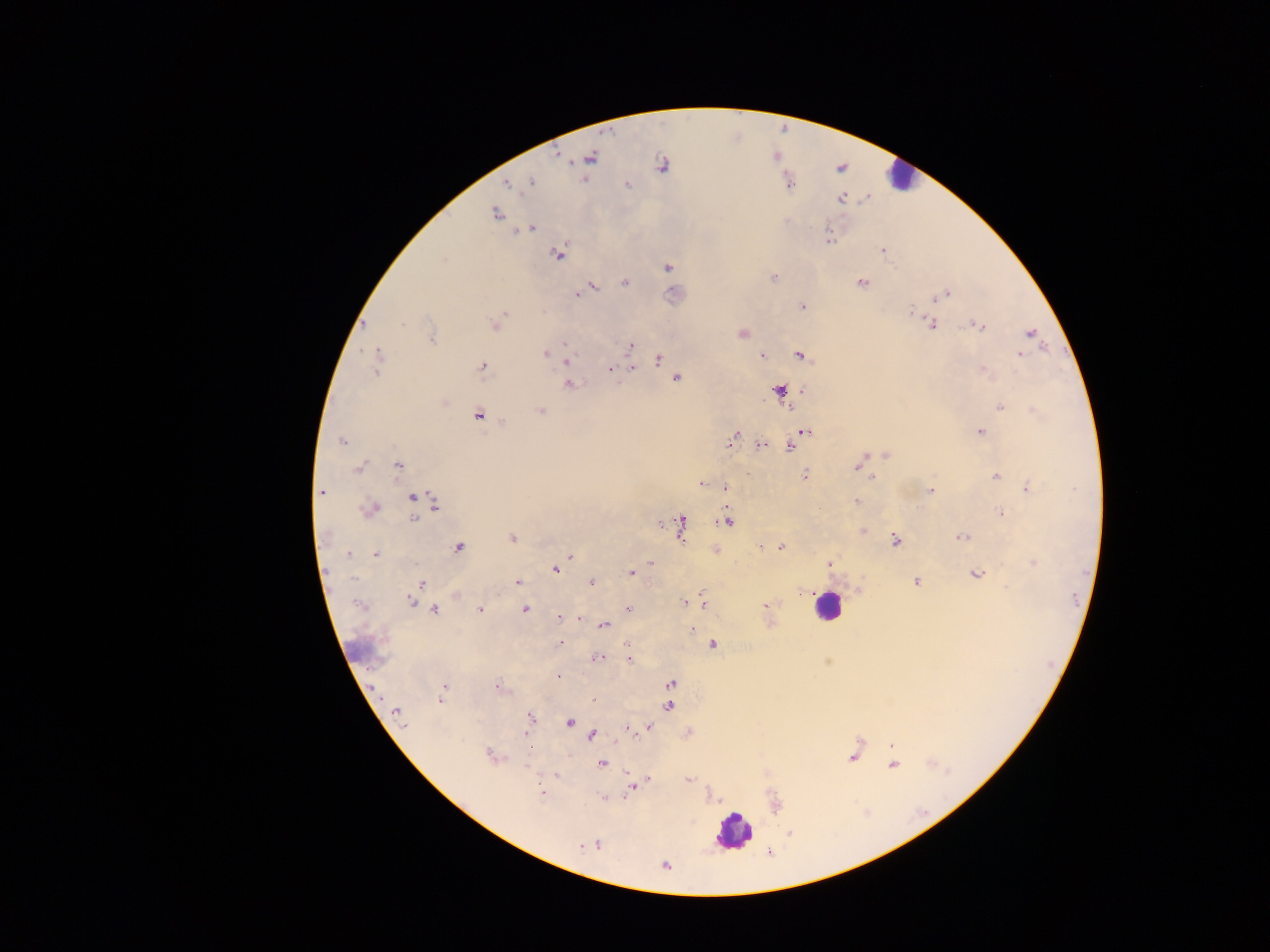

Approximate centers as (x, y) in pixels. Malaria parasite locations: (592, 157), (662, 164), (531, 183), (508, 184), (789, 184), (627, 185), (841, 198), (495, 215), (531, 228), (829, 237), (882, 251), (557, 254), (444, 259), (668, 267), (773, 277), (625, 283), (862, 283), (592, 287), (587, 290), (947, 294), (577, 295), (937, 297), (802, 307), (911, 312), (504, 313), (501, 318), (403, 324), (933, 324), (364, 325), (494, 325), (979, 326), (1029, 332), (742, 334), (432, 339), (565, 343), (630, 345), (1023, 351), (545, 353), (377, 354), (799, 355), (762, 356), (1020, 356), (659, 358), (567, 360), (482, 366), (377, 367), (631, 369), (611, 370), (982, 370), (677, 379), (568, 384), (779, 390), (802, 390), (1000, 406), (790, 409), (541, 411), (478, 414), (502, 423), (980, 431), (805, 432), (732, 438), (342, 442), (761, 446), (790, 446), (886, 454), (863, 458), (398, 465), (856, 466), (359, 467), (804, 475), (997, 476), (873, 478), (702, 484), (725, 487), (1028, 487), (321, 491), (931, 491), (412, 497), (856, 501), (435, 503), (371, 508), (820, 509), (1001, 513), (413, 519), (725, 521), (660, 524), (681, 524), (862, 530), (962, 537), (512, 539), (895, 541), (762, 547), (781, 547), (459, 548), (349, 554), (375, 554), (571, 556), (1032, 562), (650, 563), (828, 564), (555, 570), (631, 572), (977, 574), (916, 581), (518, 582), (591, 582), (421, 584), (802, 592), (456, 596), (410, 601), (685, 602), (702, 604), (765, 605), (434, 609), (480, 609), (628, 609), (525, 610), (559, 617), (579, 619), (604, 626), (692, 629), (561, 642), (712, 645), (598, 658), (629, 659), (557, 676), (671, 684), (443, 687), (497, 687), (441, 699), (593, 699), (668, 706), (397, 713), (529, 716), (570, 723), (649, 725), (627, 729), (527, 734), (592, 735), (891, 746), (489, 755), (852, 758), (602, 763), (892, 765), (557, 776), (648, 780), (688, 780), (633, 788), (541, 793), (789, 834), (598, 844), (581, 847), (664, 865). Leukocyte locations: (898, 176), (827, 606), (733, 832). Collected in Ghana. One field of view. Photographed through a microscope with a mobile-phone camera. Image is 1270×952 pixels. Thick blood film.